State which parasite is depicted.
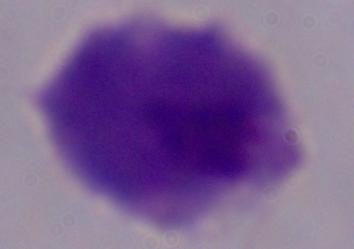

A trichomonad.

magnification = 1000x
modality = photomicrograph